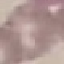

Result: no malaria parasites seen. Photographed with a smartphone camera at the microscope eyepiece. Thin blood film. Automatically extracted cell patch, resized to 64 × 64 pixels. Giemsa-stained preparation.